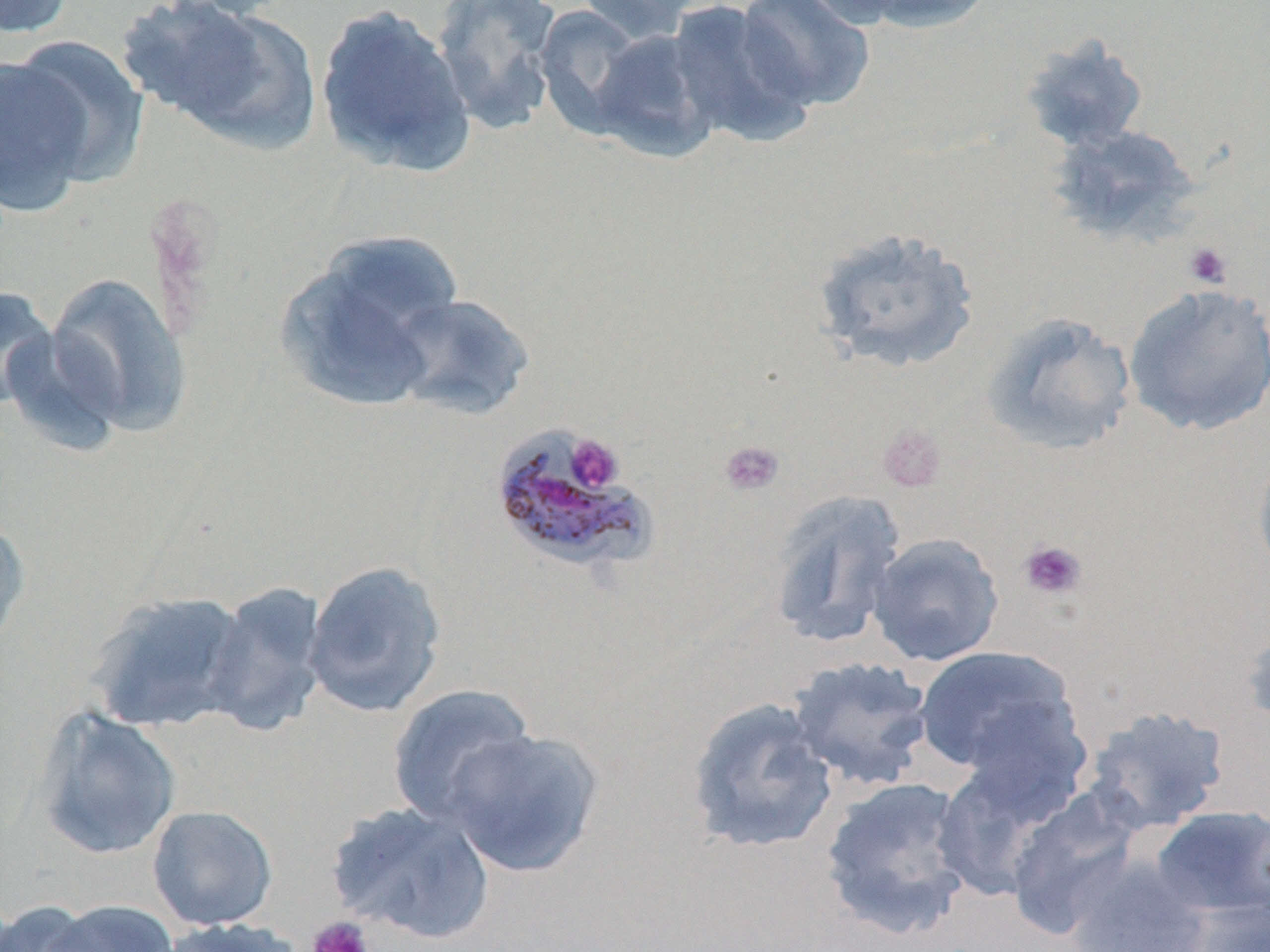

Summary:
  - Coordinate format: approximate bounding boxes as (x1,y1)-(x2,y2) corner pairs in pixels
  - Platelet locations: (1183,242)-(1232,289), (878,422)-(945,492), (565,433)-(624,492), (719,440)-(785,497), (1018,539)-(1087,601), (306,915)-(374,952)
  - Plasmodium malariae-infected red blood cell locations: (497,424)-(661,573)
  - Uninfected red blood cell locations: (0,0)-(76,39), (123,0)-(322,152), (575,0)-(707,43), (664,0)-(815,149), (841,0)-(997,33), (429,1)-(563,134), (735,1)-(875,111), (313,2)-(476,177), (533,3)-(650,136), (588,29)-(721,162), (1018,33)-(1150,153), (8,35)-(149,184), (0,55)-(95,215), (1047,123)-(1202,249), (811,225)-(980,374), (320,230)-(463,336), (43,271)-(192,437), (272,279)-(420,413), (1122,283)-(1270,437), (0,286)-(58,410), (385,292)-(536,421), (981,311)-(1138,457), (1,325)-(126,455), (1251,444)-(1270,584), (765,490)-(908,650), (0,513)-(32,653), (866,532)-(1005,667), (303,559)-(448,718), (202,580)-(330,737), (86,589)-(252,733), (1239,616)-(1270,740), (913,645)-(1086,786), (785,655)-(937,792), (386,683)-(540,827), (685,695)-(839,855), (1080,704)-(1231,835), (32,707)-(182,861), (443,728)-(605,879), (931,762)-(1059,903), (818,775)-(977,941), (1004,794)-(1143,940), (325,799)-(496,944), (146,805)-(278,931), (1151,806)-(1270,922), (1064,856)-(1212,951), (1175,896)-(1270,952), (0,899)-(105,951), (41,900)-(180,952), (158,918)-(306,952)
  - Slide-level diagnosis: Plasmodium malariae
  - Preparation: thin blood film
  - Modality: optical microscopy
  - Stain: May-Grünwald-Giemsa
  - Image size: 1270×952 pixels
  - Field of view: single
  - Magnification: 1000x